Locate and identify every blood parasite.
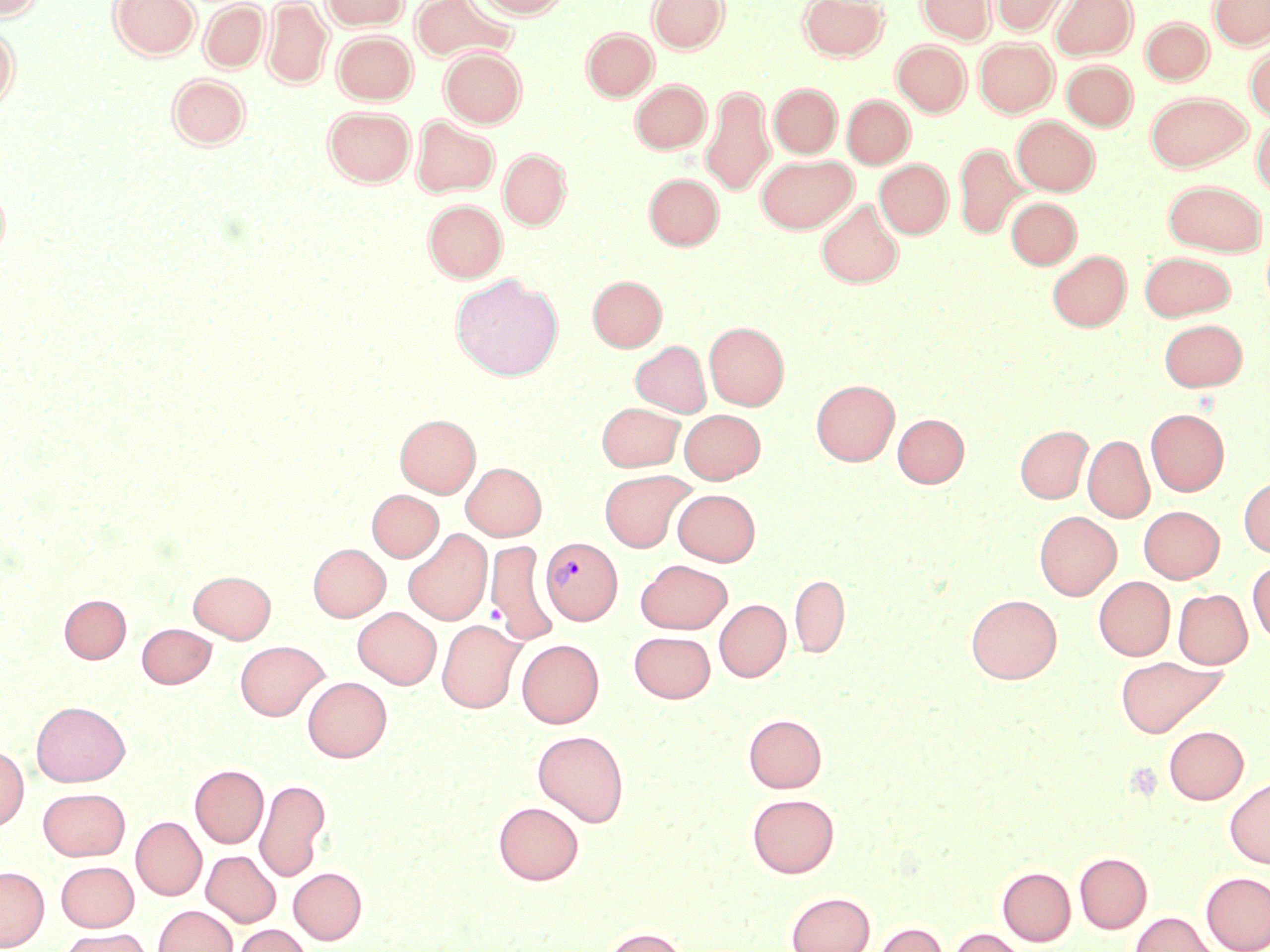

Approximate bounding boxes as named x1/y1/x2/y2 corners in pixels.
Plasmodium vivax-infected red blood cells: (x1=541, y1=537, x2=622, y2=624).
No Plasmodium falciparum, Plasmodium ovale, Plasmodium malariae, Babesia divergens, or Trypanosoma brucei observed.

Uninfected red blood cell locations: (x1=1, y1=0, x2=45, y2=22), (x1=109, y1=0, x2=199, y2=59), (x1=322, y1=0, x2=409, y2=30), (x1=410, y1=0, x2=518, y2=64), (x1=474, y1=0, x2=569, y2=18), (x1=649, y1=0, x2=729, y2=53), (x1=798, y1=0, x2=888, y2=60), (x1=918, y1=0, x2=995, y2=43), (x1=990, y1=0, x2=1069, y2=35), (x1=1051, y1=0, x2=1137, y2=59), (x1=1210, y1=0, x2=1269, y2=49), (x1=199, y1=1, x2=269, y2=72), (x1=262, y1=1, x2=332, y2=88), (x1=1141, y1=18, x2=1213, y2=84), (x1=0, y1=26, x2=18, y2=111), (x1=582, y1=28, x2=658, y2=100), (x1=332, y1=30, x2=417, y2=104), (x1=975, y1=38, x2=1057, y2=116), (x1=893, y1=41, x2=970, y2=116), (x1=1245, y1=46, x2=1270, y2=122), (x1=440, y1=47, x2=526, y2=127), (x1=1062, y1=60, x2=1137, y2=130), (x1=167, y1=73, x2=251, y2=149), (x1=631, y1=80, x2=710, y2=153), (x1=769, y1=84, x2=841, y2=157), (x1=701, y1=85, x2=775, y2=196), (x1=1146, y1=92, x2=1251, y2=171), (x1=842, y1=95, x2=914, y2=168), (x1=324, y1=106, x2=415, y2=186), (x1=411, y1=116, x2=499, y2=197), (x1=1012, y1=116, x2=1099, y2=195), (x1=1252, y1=119, x2=1270, y2=198), (x1=954, y1=142, x2=1026, y2=239), (x1=498, y1=149, x2=571, y2=229), (x1=757, y1=154, x2=856, y2=233), (x1=875, y1=159, x2=952, y2=238), (x1=644, y1=173, x2=723, y2=250), (x1=1163, y1=180, x2=1267, y2=256), (x1=0, y1=183, x2=10, y2=261), (x1=1006, y1=198, x2=1081, y2=269), (x1=423, y1=199, x2=507, y2=282), (x1=816, y1=199, x2=903, y2=288), (x1=1047, y1=250, x2=1131, y2=331), (x1=1139, y1=251, x2=1235, y2=320), (x1=451, y1=274, x2=563, y2=380), (x1=588, y1=275, x2=666, y2=352), (x1=1159, y1=319, x2=1247, y2=391), (x1=704, y1=322, x2=789, y2=410), (x1=630, y1=341, x2=711, y2=417), (x1=811, y1=380, x2=899, y2=466), (x1=597, y1=402, x2=685, y2=471), (x1=1146, y1=408, x2=1229, y2=496), (x1=679, y1=409, x2=765, y2=484), (x1=893, y1=413, x2=969, y2=487), (x1=395, y1=414, x2=480, y2=497), (x1=1015, y1=425, x2=1091, y2=503), (x1=1083, y1=434, x2=1154, y2=523), (x1=462, y1=462, x2=546, y2=540), (x1=599, y1=470, x2=696, y2=552), (x1=1238, y1=477, x2=1270, y2=557), (x1=673, y1=489, x2=760, y2=565), (x1=367, y1=490, x2=443, y2=561), (x1=1139, y1=506, x2=1224, y2=582), (x1=1035, y1=511, x2=1121, y2=600), (x1=403, y1=529, x2=492, y2=625), (x1=485, y1=540, x2=558, y2=645), (x1=308, y1=544, x2=390, y2=621), (x1=636, y1=559, x2=732, y2=633), (x1=1248, y1=559, x2=1270, y2=644), (x1=189, y1=570, x2=275, y2=643), (x1=790, y1=574, x2=849, y2=658), (x1=1094, y1=576, x2=1175, y2=660), (x1=1173, y1=589, x2=1252, y2=669), (x1=59, y1=594, x2=131, y2=663), (x1=966, y1=594, x2=1062, y2=683), (x1=715, y1=599, x2=790, y2=682), (x1=353, y1=607, x2=441, y2=689), (x1=437, y1=619, x2=525, y2=713), (x1=136, y1=623, x2=216, y2=688), (x1=629, y1=631, x2=715, y2=702), (x1=517, y1=639, x2=604, y2=728), (x1=235, y1=640, x2=329, y2=720), (x1=1115, y1=657, x2=1225, y2=737), (x1=302, y1=676, x2=391, y2=762), (x1=31, y1=701, x2=130, y2=787), (x1=743, y1=713, x2=827, y2=792), (x1=1164, y1=726, x2=1248, y2=803), (x1=532, y1=730, x2=629, y2=827), (x1=0, y1=746, x2=28, y2=830), (x1=190, y1=764, x2=268, y2=848), (x1=1225, y1=776, x2=1270, y2=868), (x1=255, y1=779, x2=330, y2=882), (x1=38, y1=788, x2=130, y2=860), (x1=747, y1=793, x2=839, y2=878), (x1=493, y1=801, x2=584, y2=885), (x1=131, y1=817, x2=206, y2=900), (x1=201, y1=850, x2=280, y2=927), (x1=1074, y1=853, x2=1152, y2=933), (x1=56, y1=861, x2=138, y2=931), (x1=0, y1=866, x2=49, y2=950), (x1=997, y1=866, x2=1076, y2=945), (x1=288, y1=867, x2=367, y2=944), (x1=1201, y1=872, x2=1270, y2=952), (x1=786, y1=891, x2=875, y2=952), (x1=153, y1=905, x2=237, y2=952), (x1=1130, y1=912, x2=1219, y2=952), (x1=873, y1=922, x2=948, y2=952), (x1=233, y1=924, x2=313, y2=952), (x1=600, y1=926, x2=688, y2=952), (x1=58, y1=927, x2=152, y2=952), (x1=948, y1=927, x2=1027, y2=952). Slide-level diagnosis: Plasmodium vivax. Captured at 1000x magnification. Optical microscopy. Thin blood smear. May-Grünwald-Giemsa stain. Image is 1270×952 pixels. One field of a larger specimen.